Describe the morphology of the erythrocytes.
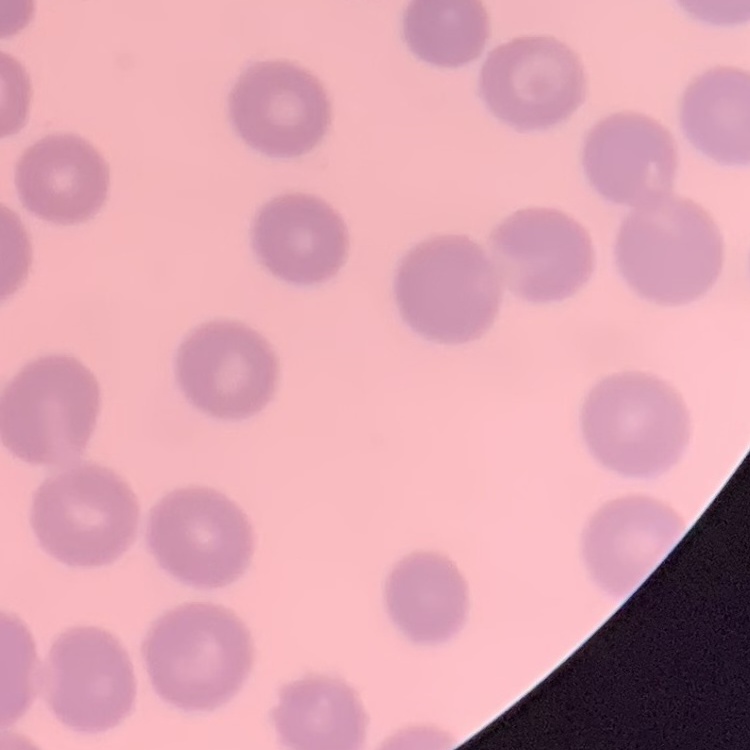

They show no rouleaux formation.

Summary:
  - Image type: one tile cut from a larger photomicrograph
  - Preparation: thin blood film
  - Stain: Field's or Giemsa